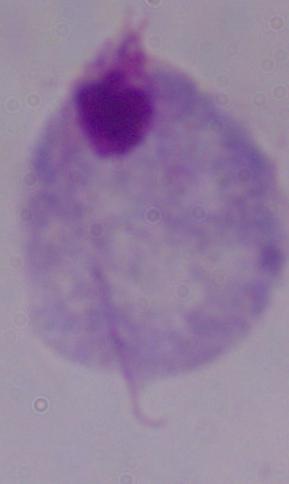

Summary:
  - Identification: trichomonad
  - Modality: micrograph
  - Magnification: 1000x